Assess this cell for malaria.
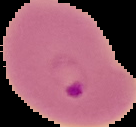

Parasitized.

From a thin blood smear. The area outside the segmented cell region is set to black. Image is 136×127 pixels.